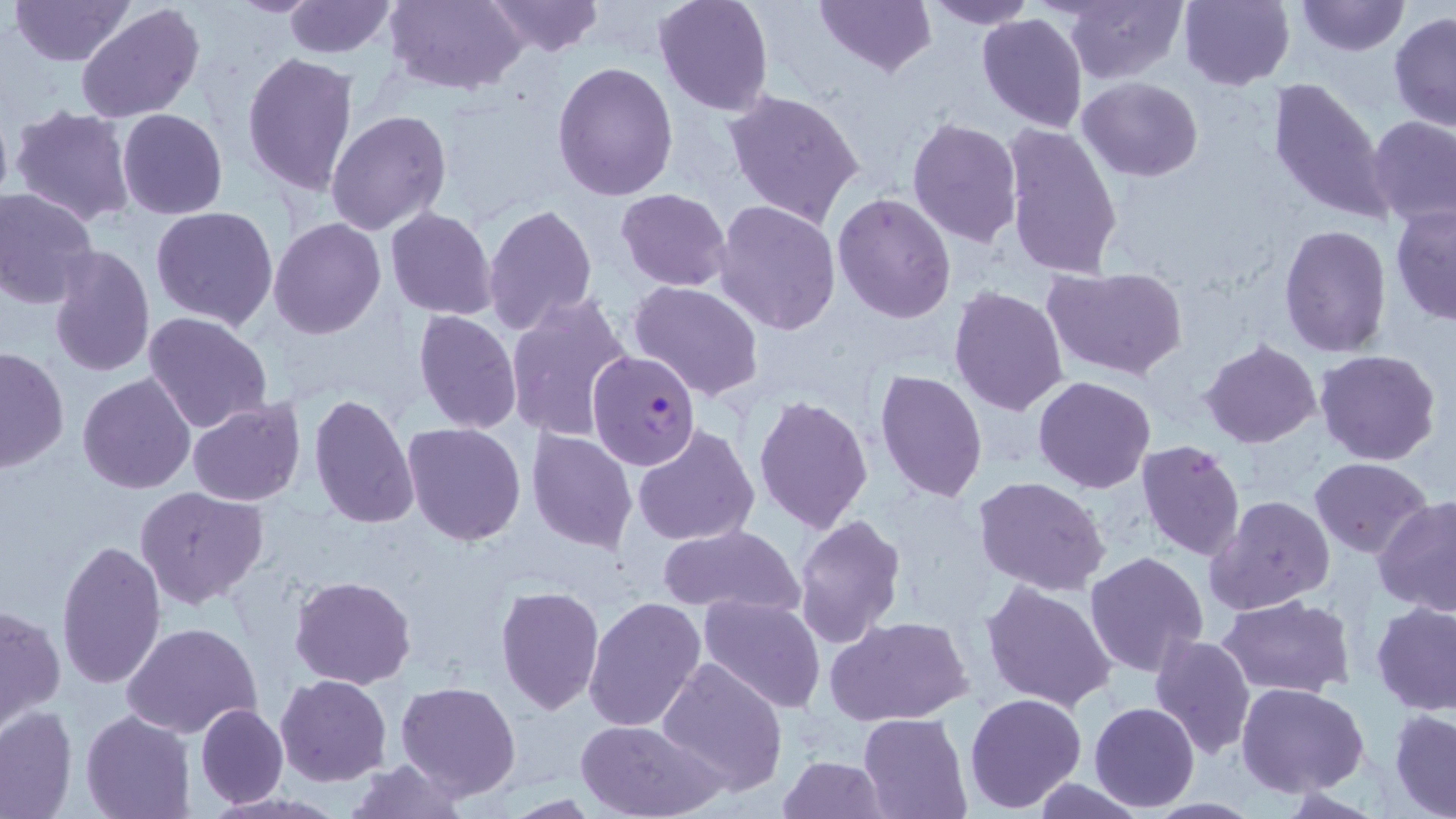

Approximate bounding boxes as named x1/y1/x2/y2 corners in pixels. Uninfected red blood cell locations: (x1=9, y1=0, x2=133, y2=66), (x1=226, y1=0, x2=327, y2=16), (x1=281, y1=0, x2=397, y2=59), (x1=384, y1=0, x2=527, y2=93), (x1=482, y1=0, x2=606, y2=56), (x1=652, y1=0, x2=774, y2=117), (x1=815, y1=0, x2=936, y2=77), (x1=924, y1=0, x2=1037, y2=28), (x1=1064, y1=0, x2=1185, y2=85), (x1=1176, y1=0, x2=1295, y2=90), (x1=1297, y1=0, x2=1406, y2=56), (x1=75, y1=4, x2=204, y2=123), (x1=1388, y1=11, x2=1456, y2=131), (x1=976, y1=12, x2=1088, y2=133), (x1=241, y1=51, x2=359, y2=197), (x1=551, y1=59, x2=678, y2=200), (x1=1266, y1=76, x2=1395, y2=227), (x1=1075, y1=77, x2=1203, y2=180), (x1=722, y1=89, x2=865, y2=229), (x1=9, y1=104, x2=138, y2=227), (x1=116, y1=108, x2=228, y2=219), (x1=325, y1=110, x2=453, y2=238), (x1=1367, y1=114, x2=1456, y2=228), (x1=907, y1=116, x2=1023, y2=248), (x1=1001, y1=122, x2=1126, y2=279), (x1=0, y1=187, x2=100, y2=309), (x1=615, y1=188, x2=734, y2=291), (x1=833, y1=191, x2=959, y2=323), (x1=713, y1=200, x2=843, y2=336), (x1=1390, y1=203, x2=1456, y2=325), (x1=482, y1=204, x2=598, y2=339), (x1=386, y1=206, x2=499, y2=319), (x1=150, y1=207, x2=279, y2=331), (x1=268, y1=218, x2=386, y2=339), (x1=1278, y1=224, x2=1392, y2=357), (x1=47, y1=245, x2=156, y2=379), (x1=1043, y1=266, x2=1187, y2=382), (x1=627, y1=281, x2=766, y2=402), (x1=948, y1=286, x2=1070, y2=415), (x1=504, y1=293, x2=637, y2=441), (x1=413, y1=308, x2=521, y2=434), (x1=142, y1=311, x2=273, y2=436), (x1=1201, y1=339, x2=1321, y2=449), (x1=0, y1=345, x2=71, y2=472), (x1=1314, y1=348, x2=1441, y2=465), (x1=874, y1=369, x2=990, y2=505), (x1=77, y1=372, x2=198, y2=494), (x1=1033, y1=376, x2=1156, y2=493), (x1=308, y1=393, x2=420, y2=531), (x1=752, y1=395, x2=873, y2=534), (x1=188, y1=397, x2=307, y2=506), (x1=403, y1=423, x2=527, y2=547), (x1=632, y1=425, x2=762, y2=548), (x1=526, y1=428, x2=636, y2=552), (x1=1136, y1=438, x2=1247, y2=564), (x1=1309, y1=457, x2=1431, y2=556), (x1=973, y1=476, x2=1110, y2=595), (x1=137, y1=487, x2=268, y2=608), (x1=1204, y1=495, x2=1334, y2=617), (x1=1374, y1=498, x2=1456, y2=617), (x1=793, y1=512, x2=907, y2=648), (x1=656, y1=523, x2=805, y2=617), (x1=55, y1=537, x2=168, y2=690), (x1=1084, y1=551, x2=1210, y2=679), (x1=290, y1=575, x2=416, y2=690), (x1=980, y1=580, x2=1117, y2=712), (x1=495, y1=585, x2=605, y2=715), (x1=585, y1=595, x2=707, y2=734), (x1=698, y1=595, x2=824, y2=714), (x1=1216, y1=595, x2=1354, y2=696), (x1=1372, y1=601, x2=1456, y2=714), (x1=1, y1=602, x2=65, y2=732), (x1=825, y1=613, x2=973, y2=727), (x1=121, y1=621, x2=262, y2=738), (x1=1148, y1=631, x2=1257, y2=759), (x1=656, y1=655, x2=789, y2=796), (x1=274, y1=674, x2=392, y2=787), (x1=396, y1=681, x2=520, y2=800), (x1=1237, y1=683, x2=1369, y2=799), (x1=964, y1=692, x2=1087, y2=811), (x1=195, y1=702, x2=288, y2=808), (x1=1089, y1=702, x2=1200, y2=813), (x1=0, y1=705, x2=78, y2=819), (x1=81, y1=708, x2=195, y2=819), (x1=1390, y1=708, x2=1456, y2=817), (x1=859, y1=712, x2=971, y2=819), (x1=574, y1=718, x2=725, y2=819), (x1=779, y1=755, x2=889, y2=818), (x1=342, y1=758, x2=469, y2=818). Plasmodium falciparum-infected red blood cell locations: (x1=587, y1=350, x2=703, y2=472). Slide-level diagnosis: Plasmodium falciparum. Optical microscopy. One field of a larger specimen. Image is 1456×819 pixels. Captured at 1000x magnification. Thin blood smear. May-Grünwald-Giemsa stain.